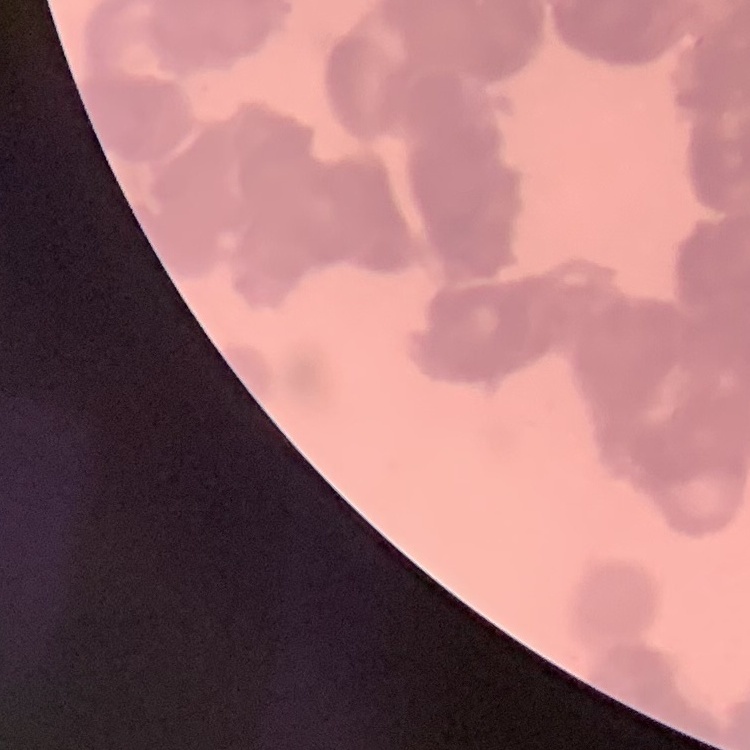

red blood cell morphology = rouleaux formation
stain = Field's or Giemsa
preparation = thin blood smear
image type = square crop of a larger photomicrograph